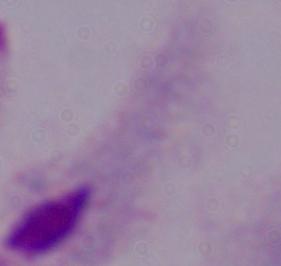
identification = trichomonad
modality = micrograph
magnification = 1000x